Classify this cell by malaria status.
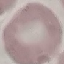
It is uninfected.

Thin smear of blood. Automatically extracted cell patch, resized to 64 × 64 pixels. Acquired by smartphone through the microscope eyepiece. Giemsa stain.